Locate every blood parasite and identify its species.
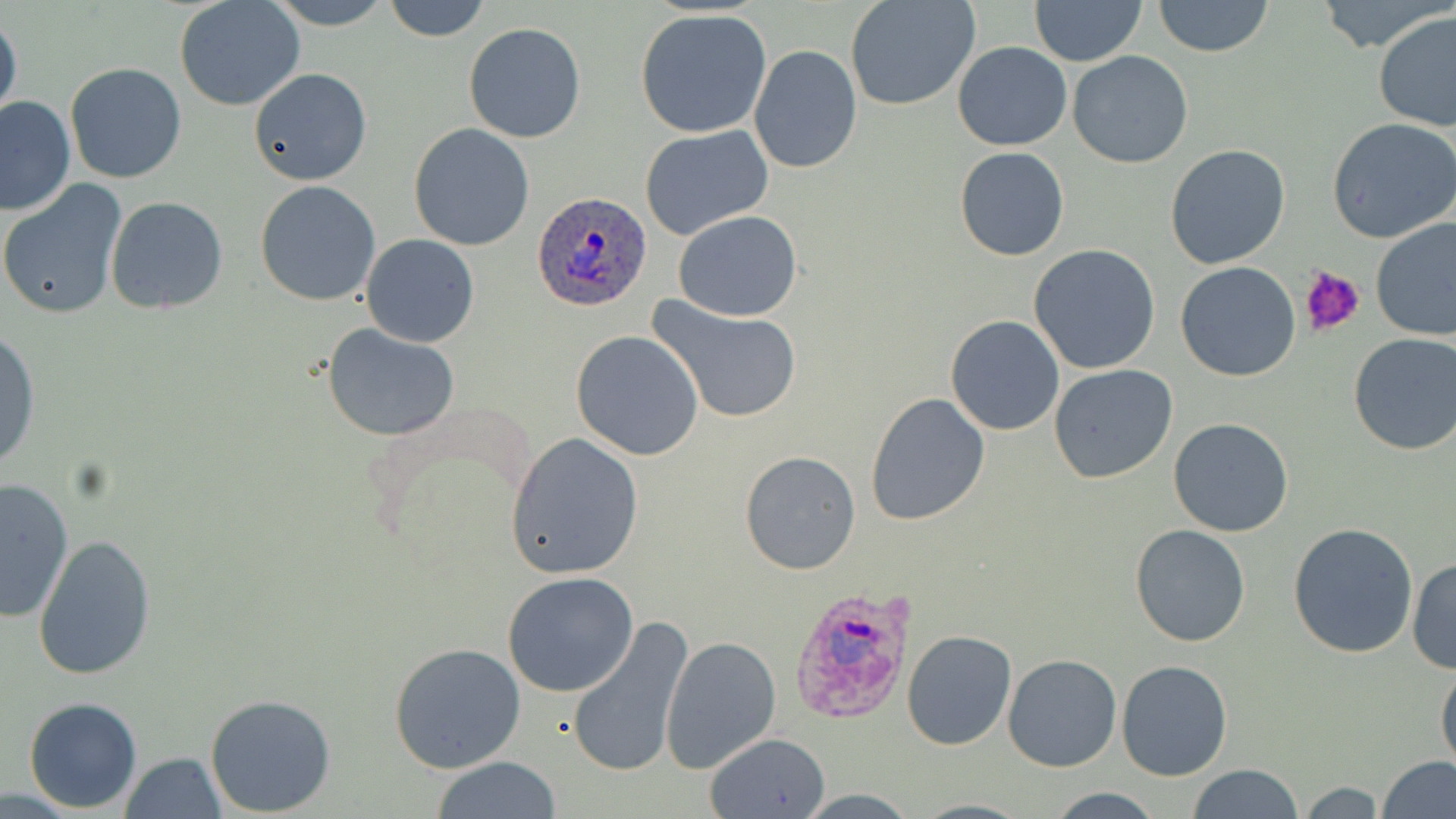

Approximate bounding boxes as named x1/y1/x2/y2 corners in pixels.
Plasmodium ovale-infected red blood cells: (x1=532, y1=190, x2=652, y2=312), (x1=791, y1=583, x2=920, y2=726).
No Plasmodium falciparum, Plasmodium malariae, Plasmodium vivax, Babesia divergens, or Trypanosoma brucei observed.

slide-level diagnosis = Plasmodium ovale
platelet locations = approximate bounding boxes as named x1/y1/x2/y2 corners in pixels: (x1=1300, y1=267, x2=1366, y2=338)
image size = 1456×819 pixels
magnification = 1000x
stain = May-Grünwald-Giemsa
uninfected red blood cell locations = approximate bounding boxes as named x1/y1/x2/y2 corners in pixels: (x1=262, y1=0, x2=397, y2=29), (x1=383, y1=0, x2=490, y2=41), (x1=845, y1=0, x2=983, y2=111), (x1=1029, y1=0, x2=1146, y2=65), (x1=1152, y1=0, x2=1274, y2=57), (x1=174, y1=1, x2=305, y2=112), (x1=634, y1=9, x2=772, y2=138), (x1=1373, y1=9, x2=1455, y2=131), (x1=0, y1=12, x2=23, y2=125), (x1=463, y1=21, x2=586, y2=142), (x1=953, y1=41, x2=1072, y2=150), (x1=749, y1=44, x2=862, y2=174), (x1=1067, y1=51, x2=1194, y2=169), (x1=66, y1=62, x2=186, y2=184), (x1=250, y1=67, x2=372, y2=186), (x1=1, y1=95, x2=73, y2=213), (x1=1326, y1=118, x2=1456, y2=243), (x1=407, y1=122, x2=535, y2=251), (x1=640, y1=126, x2=774, y2=242), (x1=1165, y1=143, x2=1291, y2=269), (x1=954, y1=146, x2=1069, y2=260), (x1=0, y1=179, x2=129, y2=321), (x1=255, y1=180, x2=382, y2=304), (x1=105, y1=196, x2=230, y2=315), (x1=672, y1=210, x2=803, y2=322), (x1=1370, y1=217, x2=1456, y2=341), (x1=360, y1=234, x2=481, y2=348), (x1=1028, y1=244, x2=1162, y2=375), (x1=1175, y1=262, x2=1302, y2=382), (x1=648, y1=298, x2=804, y2=425), (x1=945, y1=315, x2=1065, y2=435), (x1=322, y1=325, x2=459, y2=441), (x1=0, y1=328, x2=40, y2=471), (x1=572, y1=330, x2=704, y2=460), (x1=1347, y1=332, x2=1456, y2=456), (x1=1049, y1=365, x2=1179, y2=484), (x1=865, y1=391, x2=991, y2=526), (x1=359, y1=400, x2=542, y2=578), (x1=1168, y1=417, x2=1294, y2=537), (x1=505, y1=432, x2=645, y2=580), (x1=738, y1=450, x2=861, y2=576), (x1=0, y1=477, x2=74, y2=622), (x1=1287, y1=521, x2=1420, y2=657), (x1=1130, y1=523, x2=1252, y2=648), (x1=33, y1=534, x2=157, y2=680), (x1=1408, y1=557, x2=1456, y2=674), (x1=503, y1=572, x2=640, y2=697), (x1=566, y1=617, x2=694, y2=778), (x1=901, y1=630, x2=1017, y2=750), (x1=661, y1=636, x2=781, y2=773), (x1=388, y1=641, x2=528, y2=774), (x1=1003, y1=654, x2=1123, y2=772), (x1=1436, y1=659, x2=1456, y2=775), (x1=1116, y1=660, x2=1233, y2=780), (x1=206, y1=694, x2=336, y2=816), (x1=23, y1=697, x2=142, y2=811), (x1=704, y1=731, x2=832, y2=819), (x1=120, y1=752, x2=227, y2=818), (x1=1374, y1=755, x2=1456, y2=819), (x1=432, y1=757, x2=564, y2=817), (x1=1188, y1=763, x2=1304, y2=819), (x1=1298, y1=780, x2=1385, y2=816), (x1=1047, y1=787, x2=1166, y2=818), (x1=795, y1=788, x2=921, y2=817), (x1=911, y1=798, x2=1036, y2=818)
modality = light microscopy
preparation = thin blood film
field of view = single